Give the extent of all Plasmodium vivax-infected red blood cells.
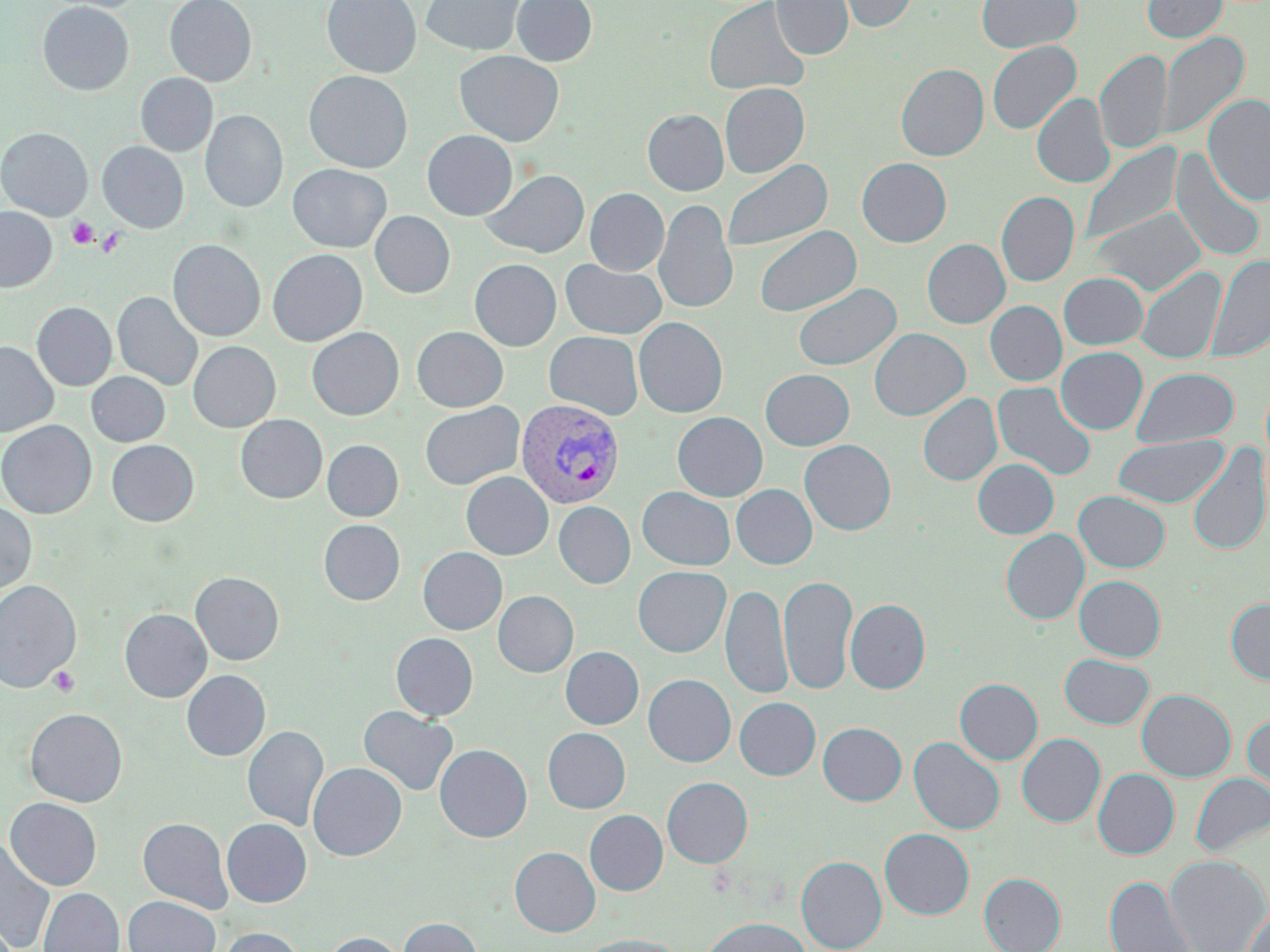

Approximate bounding boxes as named x1/y1/x2/y2 corners in pixels.
Plasmodium vivax-infected red blood cells: (x1=515, y1=398, x2=625, y2=509).

Platelet locations: (x1=68, y1=218, x2=98, y2=248), (x1=96, y1=227, x2=125, y2=258), (x1=48, y1=666, x2=80, y2=697). Uninfected red blood cell locations: (x1=164, y1=0, x2=257, y2=86), (x1=321, y1=0, x2=421, y2=78), (x1=421, y1=0, x2=524, y2=56), (x1=512, y1=0, x2=597, y2=66), (x1=703, y1=0, x2=811, y2=97), (x1=771, y1=0, x2=853, y2=60), (x1=835, y1=0, x2=918, y2=33), (x1=976, y1=0, x2=1082, y2=54), (x1=1142, y1=0, x2=1227, y2=43), (x1=37, y1=2, x2=134, y2=95), (x1=1157, y1=31, x2=1249, y2=141), (x1=986, y1=40, x2=1081, y2=135), (x1=1095, y1=49, x2=1172, y2=156), (x1=454, y1=50, x2=564, y2=146), (x1=896, y1=63, x2=988, y2=161), (x1=304, y1=71, x2=413, y2=173), (x1=136, y1=73, x2=218, y2=157), (x1=719, y1=83, x2=810, y2=178), (x1=1032, y1=93, x2=1115, y2=189), (x1=1202, y1=94, x2=1270, y2=206), (x1=642, y1=109, x2=729, y2=196), (x1=201, y1=110, x2=288, y2=212), (x1=0, y1=127, x2=93, y2=220), (x1=422, y1=130, x2=518, y2=220), (x1=98, y1=141, x2=189, y2=232), (x1=1079, y1=142, x2=1183, y2=248), (x1=1170, y1=151, x2=1267, y2=262), (x1=856, y1=157, x2=951, y2=247), (x1=721, y1=159, x2=833, y2=254), (x1=288, y1=164, x2=392, y2=252), (x1=481, y1=169, x2=589, y2=258), (x1=585, y1=188, x2=669, y2=275), (x1=997, y1=191, x2=1079, y2=287), (x1=653, y1=199, x2=739, y2=317), (x1=0, y1=206, x2=57, y2=292), (x1=1088, y1=206, x2=1206, y2=297), (x1=370, y1=211, x2=455, y2=298), (x1=755, y1=225, x2=862, y2=317), (x1=922, y1=239, x2=1010, y2=328), (x1=167, y1=240, x2=266, y2=341), (x1=267, y1=249, x2=368, y2=346), (x1=1206, y1=254, x2=1270, y2=363), (x1=469, y1=259, x2=561, y2=351), (x1=560, y1=259, x2=668, y2=340), (x1=1135, y1=266, x2=1227, y2=365), (x1=1059, y1=272, x2=1149, y2=350), (x1=792, y1=283, x2=902, y2=372), (x1=113, y1=291, x2=203, y2=391), (x1=985, y1=301, x2=1067, y2=386), (x1=31, y1=302, x2=116, y2=390), (x1=633, y1=317, x2=728, y2=418), (x1=411, y1=326, x2=508, y2=412), (x1=306, y1=327, x2=404, y2=420), (x1=869, y1=328, x2=970, y2=420), (x1=544, y1=331, x2=643, y2=420), (x1=0, y1=340, x2=58, y2=437), (x1=188, y1=341, x2=281, y2=432), (x1=1056, y1=347, x2=1148, y2=435), (x1=1131, y1=367, x2=1239, y2=448), (x1=760, y1=369, x2=855, y2=451), (x1=86, y1=372, x2=170, y2=446), (x1=992, y1=381, x2=1097, y2=482), (x1=918, y1=393, x2=1002, y2=486), (x1=420, y1=401, x2=524, y2=490), (x1=672, y1=412, x2=768, y2=501), (x1=235, y1=414, x2=327, y2=503), (x1=0, y1=420, x2=96, y2=518), (x1=1112, y1=435, x2=1228, y2=508), (x1=322, y1=439, x2=403, y2=521), (x1=106, y1=440, x2=199, y2=526), (x1=799, y1=440, x2=896, y2=535), (x1=1186, y1=444, x2=1270, y2=557), (x1=973, y1=459, x2=1058, y2=539), (x1=461, y1=471, x2=553, y2=560), (x1=731, y1=484, x2=817, y2=569), (x1=637, y1=487, x2=735, y2=570), (x1=1074, y1=490, x2=1170, y2=573), (x1=0, y1=501, x2=36, y2=598), (x1=553, y1=501, x2=636, y2=589), (x1=318, y1=519, x2=405, y2=605), (x1=1001, y1=529, x2=1089, y2=625), (x1=417, y1=547, x2=507, y2=635), (x1=632, y1=566, x2=731, y2=657), (x1=190, y1=571, x2=284, y2=665), (x1=779, y1=575, x2=858, y2=695), (x1=1074, y1=575, x2=1165, y2=661), (x1=0, y1=580, x2=82, y2=693), (x1=721, y1=583, x2=790, y2=700), (x1=493, y1=591, x2=578, y2=677), (x1=845, y1=598, x2=930, y2=694), (x1=1226, y1=599, x2=1270, y2=685), (x1=120, y1=608, x2=211, y2=702), (x1=391, y1=633, x2=478, y2=721), (x1=560, y1=646, x2=643, y2=729), (x1=1059, y1=653, x2=1155, y2=729), (x1=181, y1=670, x2=270, y2=761), (x1=643, y1=674, x2=735, y2=767), (x1=954, y1=678, x2=1042, y2=765), (x1=1136, y1=689, x2=1236, y2=781), (x1=734, y1=697, x2=820, y2=780), (x1=358, y1=706, x2=458, y2=797), (x1=24, y1=708, x2=127, y2=807), (x1=1242, y1=712, x2=1270, y2=805), (x1=818, y1=722, x2=907, y2=806), (x1=242, y1=725, x2=329, y2=831), (x1=543, y1=728, x2=630, y2=813), (x1=1017, y1=733, x2=1105, y2=827), (x1=909, y1=736, x2=1005, y2=835), (x1=434, y1=744, x2=532, y2=842), (x1=308, y1=762, x2=406, y2=860), (x1=1093, y1=768, x2=1180, y2=859), (x1=1191, y1=773, x2=1270, y2=856), (x1=662, y1=777, x2=753, y2=868), (x1=4, y1=797, x2=102, y2=890), (x1=584, y1=809, x2=668, y2=895), (x1=137, y1=817, x2=232, y2=913), (x1=221, y1=818, x2=311, y2=907), (x1=879, y1=828, x2=974, y2=919), (x1=0, y1=838, x2=56, y2=952), (x1=510, y1=846, x2=600, y2=937), (x1=1163, y1=854, x2=1270, y2=952), (x1=796, y1=856, x2=887, y2=952), (x1=979, y1=872, x2=1066, y2=952), (x1=1104, y1=875, x2=1198, y2=952), (x1=38, y1=887, x2=124, y2=952), (x1=123, y1=895, x2=220, y2=952), (x1=1242, y1=901, x2=1270, y2=952), (x1=701, y1=916, x2=811, y2=952), (x1=398, y1=917, x2=482, y2=952), (x1=217, y1=926, x2=306, y2=952), (x1=321, y1=932, x2=406, y2=952), (x1=575, y1=934, x2=687, y2=952). Slide-level diagnosis: Plasmodium vivax. Optical microscopy. May-Grünwald-Giemsa stain. One field of a larger specimen. Image is 1270×952 pixels. 1000x magnification. Thin blood film.